Identify the parasite.
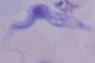
A trypanosome.

Photomicrograph. Captured at 1000x magnification.